Locate and identify every blood parasite.
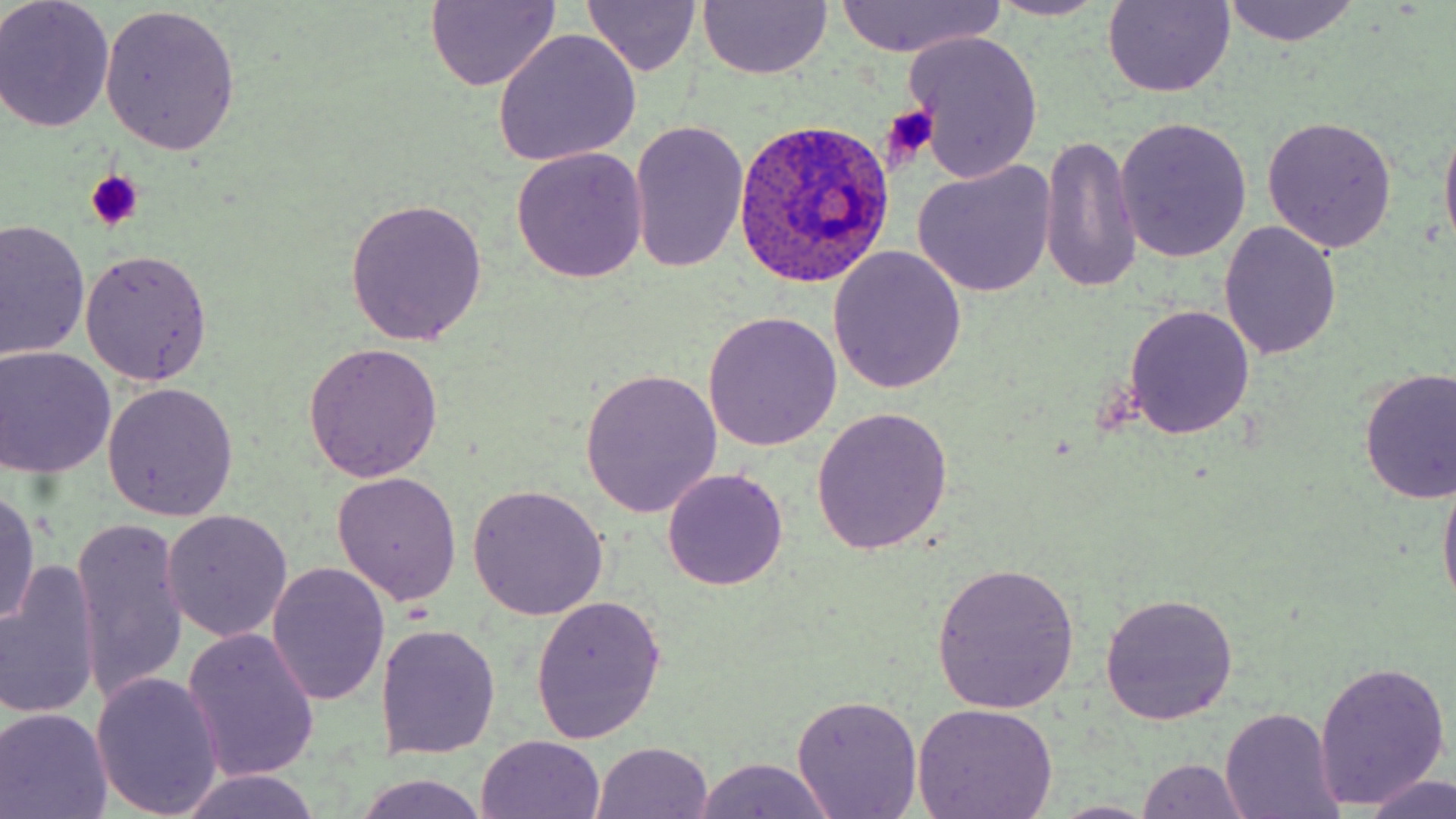
Approximate bounding boxes as named x1/y1/x2/y2 corners in pixels.
Plasmodium ovale-infected red blood cells: (x1=733, y1=118, x2=895, y2=289).
No Plasmodium falciparum, Plasmodium malariae, Plasmodium vivax, Babesia divergens, or Trypanosoma brucei observed.

slide-level diagnosis = Plasmodium ovale
image size = 1456×819 pixels
uninfected red blood cell locations = approximate bounding boxes as named x1/y1/x2/y2 corners in pixels: (x1=0, y1=0, x2=116, y2=132), (x1=982, y1=0, x2=1115, y2=21), (x1=424, y1=1, x2=562, y2=90), (x1=1100, y1=1, x2=1237, y2=98), (x1=1219, y1=1, x2=1361, y2=46), (x1=697, y1=2, x2=832, y2=80), (x1=829, y1=2, x2=1006, y2=57), (x1=583, y1=3, x2=704, y2=77), (x1=99, y1=4, x2=241, y2=153), (x1=492, y1=29, x2=642, y2=166), (x1=903, y1=31, x2=1046, y2=184), (x1=1438, y1=110, x2=1456, y2=265), (x1=1261, y1=116, x2=1396, y2=254), (x1=1115, y1=117, x2=1252, y2=263), (x1=627, y1=122, x2=748, y2=274), (x1=1038, y1=136, x2=1144, y2=295), (x1=511, y1=146, x2=648, y2=284), (x1=912, y1=161, x2=1057, y2=298), (x1=347, y1=198, x2=490, y2=345), (x1=1, y1=218, x2=90, y2=365), (x1=1219, y1=221, x2=1342, y2=360), (x1=827, y1=246, x2=967, y2=395), (x1=80, y1=249, x2=213, y2=385), (x1=1123, y1=304, x2=1256, y2=440), (x1=703, y1=309, x2=843, y2=452), (x1=301, y1=343, x2=442, y2=483), (x1=0, y1=346, x2=116, y2=478), (x1=1356, y1=367, x2=1456, y2=506), (x1=580, y1=368, x2=722, y2=517), (x1=102, y1=382, x2=239, y2=521), (x1=810, y1=405, x2=955, y2=553), (x1=1438, y1=463, x2=1456, y2=617), (x1=663, y1=469, x2=786, y2=589), (x1=330, y1=470, x2=463, y2=605), (x1=467, y1=485, x2=609, y2=620), (x1=0, y1=488, x2=42, y2=631), (x1=160, y1=512, x2=293, y2=644), (x1=71, y1=520, x2=191, y2=705), (x1=929, y1=560, x2=1081, y2=711), (x1=1, y1=561, x2=101, y2=723), (x1=267, y1=564, x2=390, y2=705), (x1=1098, y1=592, x2=1238, y2=723), (x1=530, y1=596, x2=667, y2=744), (x1=378, y1=623, x2=499, y2=759), (x1=182, y1=627, x2=321, y2=784), (x1=1315, y1=660, x2=1451, y2=810), (x1=91, y1=672, x2=224, y2=817), (x1=791, y1=694, x2=924, y2=819), (x1=911, y1=703, x2=1061, y2=819), (x1=0, y1=706, x2=114, y2=819), (x1=1219, y1=708, x2=1343, y2=819), (x1=476, y1=734, x2=606, y2=819), (x1=591, y1=742, x2=715, y2=819), (x1=688, y1=756, x2=840, y2=818), (x1=1134, y1=758, x2=1253, y2=818), (x1=177, y1=769, x2=323, y2=819), (x1=351, y1=772, x2=493, y2=819), (x1=1362, y1=773, x2=1456, y2=819), (x1=1047, y1=800, x2=1161, y2=818)
platelet locations = approximate bounding boxes as named x1/y1/x2/y2 corners in pixels: (x1=880, y1=106, x2=938, y2=166), (x1=85, y1=170, x2=144, y2=231)
preparation = thin blood smear
stain = May-Grünwald-Giemsa
modality = light microscopy
field of view = one of a larger specimen
magnification = 1000x